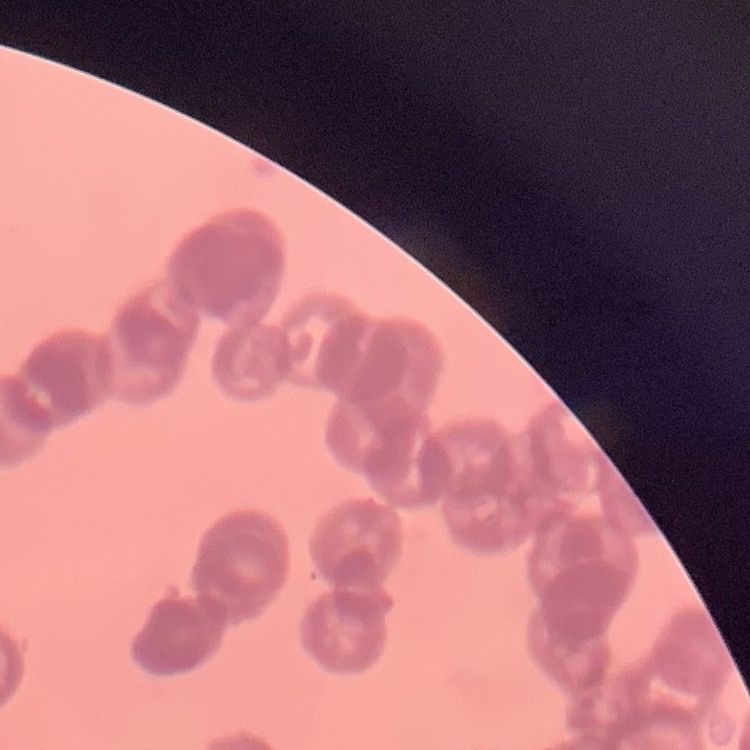

Summary:
  - Red blood cell morphology: rouleaux formation
  - Image type: square crop of a larger photomicrograph
  - Preparation: thin peripheral smear
  - Stain: Field's or Giemsa